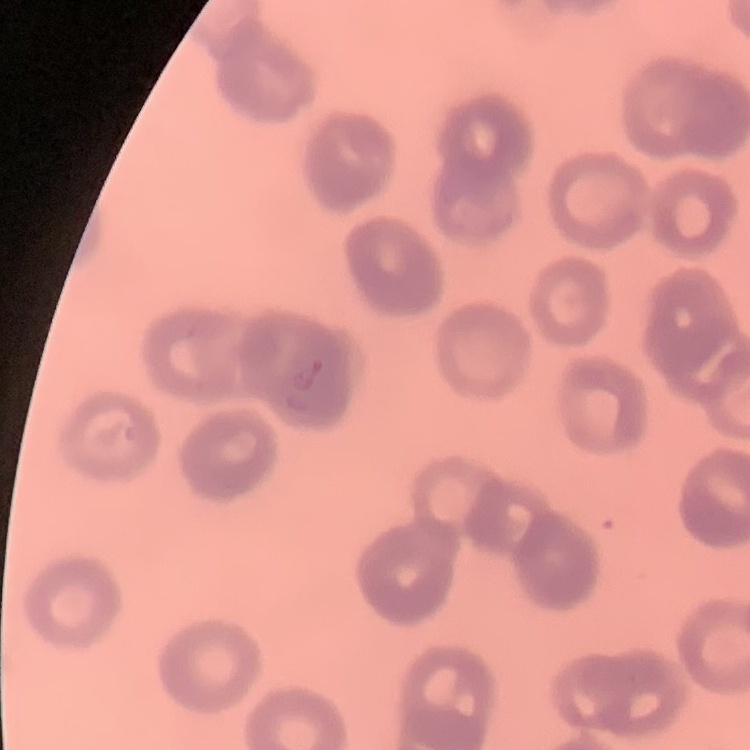

Summary:
  - Erythrocyte morphology: rouleaux formation
  - Stain: Field's or Giemsa
  - Preparation: thin peripheral smear
  - Image type: square crop of a larger photomicrograph